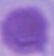

identification = erythrocyte
modality = photomicrograph
magnification = 1000x